Classify this cell by malaria status.
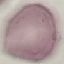
Uninfected.

stain = Giemsa
capture = smartphone through the microscope eyepiece
preparation = thin smear
image type = automatically extracted cell patch, resized to 64 × 64 pixels